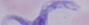
Summary:
  - Magnification: 1000x
  - Modality: photomicrograph
  - Identification: trypanosome